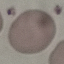
{
  "result": "negative for malaria parasites",
  "image_type": "cell patch, automatically extracted from a larger field of view and resized to 64 × 64 pixels",
  "preparation": "thin smear",
  "capture": "smartphone camera at the microscope eyepiece",
  "stain": "Giemsa"
}